Describe the morphology of the red blood cells.
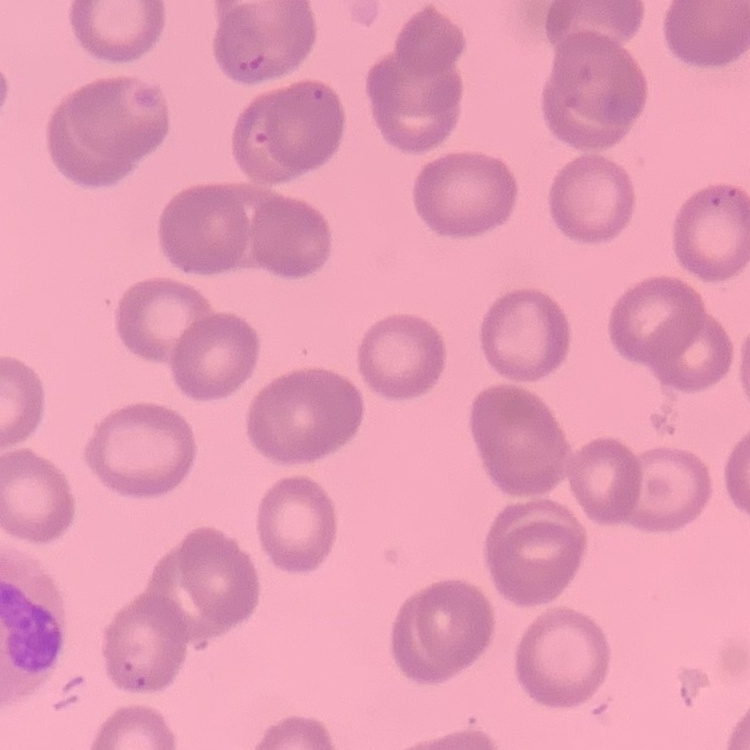
No rouleaux formation.

Summary:
  - Image type: square crop of a larger photomicrograph
  - Preparation: thin blood smear
  - Stain: Field's or Giemsa